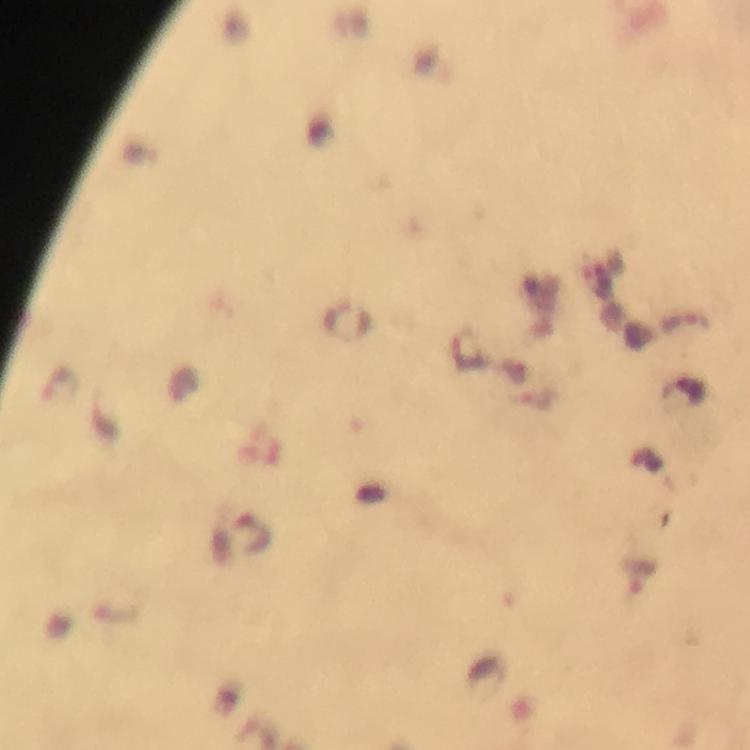 Approximate centers as (x, y) in pixels. Plasmodium parasite locations: (347, 319), (687, 323), (59, 384), (250, 535), (637, 577). Thick blood smear. Immersion oil applied. Image is 750×750 pixels. Giemsa stain. From a malaria diagnostic workup. 100x magnification. A crop from one field of view. Photographed with a smartphone mounted on the microscope.